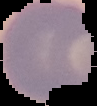

Summary:
  - Result: no malaria parasites detected
  - Image type: cell region segmented out of the field of view; surrounding area masked to black
  - Preparation: thin blood film
  - Image size: 97×106 pixels